Assess this cell for malaria.
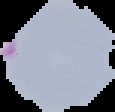
Parasitized.

Summary:
  - Image type: cell region segmented out of the field of view; surrounding area masked to black
  - Image size: 115×112 pixels
  - Preparation: thin blood smear